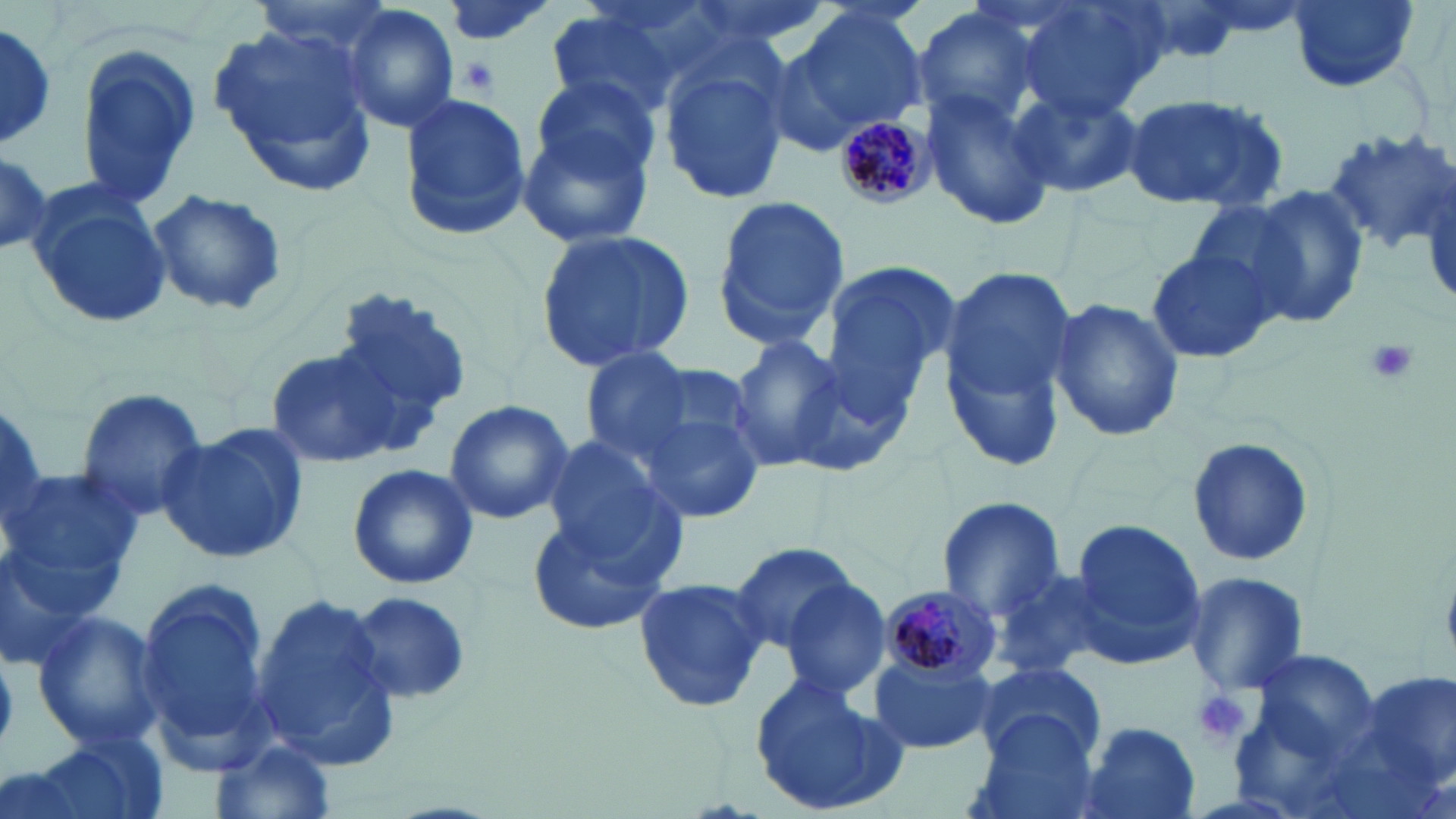
Summary:
  - Coordinate format: approximate bounding boxes as [x1, y1, x2, y2] in pixels
  - Platelet locations: [457, 56, 497, 96], [1361, 335, 1420, 387], [1190, 687, 1255, 748]
  - Uninfected red blood cell locations: [433, 0, 559, 48], [1011, 0, 1170, 120], [1287, 0, 1418, 92], [770, 4, 930, 150], [912, 4, 1055, 136], [340, 5, 461, 134], [544, 8, 692, 115], [209, 20, 378, 189], [0, 24, 59, 149], [75, 46, 201, 210], [657, 49, 791, 204], [516, 80, 663, 245], [1010, 86, 1145, 200], [922, 88, 1060, 229], [396, 91, 535, 240], [1119, 93, 1292, 209], [1322, 128, 1456, 255], [0, 144, 50, 256], [28, 185, 169, 327], [1247, 188, 1370, 327], [146, 189, 289, 318], [1186, 193, 1325, 322], [709, 194, 851, 354], [534, 226, 697, 374], [1144, 241, 1281, 366], [817, 262, 956, 418], [937, 265, 1086, 465], [325, 284, 475, 438], [1050, 298, 1185, 442], [725, 336, 849, 473], [577, 346, 700, 461], [267, 349, 395, 470], [73, 386, 207, 522], [635, 394, 767, 526], [443, 398, 573, 525], [161, 422, 309, 565], [541, 433, 683, 570], [1185, 434, 1315, 569], [346, 462, 479, 590], [4, 463, 145, 602], [935, 496, 1067, 621], [524, 510, 675, 639], [1064, 515, 1207, 667], [727, 544, 864, 657], [0, 545, 108, 672], [989, 565, 1122, 678], [1183, 572, 1308, 697], [632, 575, 771, 715], [781, 578, 893, 701], [347, 589, 476, 708], [135, 590, 276, 759], [253, 592, 400, 769], [30, 609, 163, 753], [1235, 642, 1385, 794], [869, 655, 996, 756], [971, 660, 1106, 767], [1342, 665, 1453, 811], [749, 671, 907, 816], [967, 714, 1101, 819], [1073, 719, 1201, 819], [26, 731, 168, 819], [211, 734, 337, 819]
  - Plasmodium malariae-infected red blood cell locations: [834, 112, 932, 210], [878, 586, 1000, 690]
  - Slide-level diagnosis: Plasmodium malariae
  - Preparation: thin blood smear
  - Magnification: 1000x
  - Stain: May-Grünwald-Giemsa
  - Field of view: single
  - Modality: light microscopy
  - Image size: 1456×819 pixels